Report the malaria status of this cell.
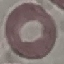

It is uninfected.

capture: smartphone through the microscope eyepiece
image_type: automatically extracted cell patch, resized to 64 × 64 pixels
stain: Giemsa
preparation: thin blood film